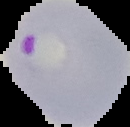
Malaria status: parasitized. From a thin blood film. Cell region segmented out of the field of view; the surrounding area is masked to black. Image is 130×127 pixels.